Describe the morphology of the erythrocytes.
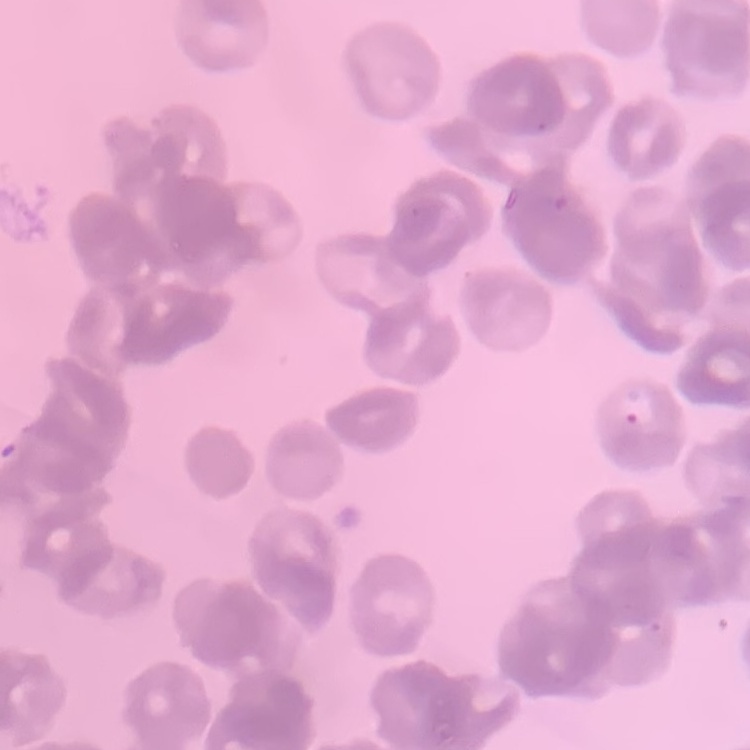

They show rouleaux formation.

Summary:
  - Image type: square crop of a larger photomicrograph
  - Preparation: thin blood film
  - Stain: Field's or Giemsa